Locate every malaria parasite.
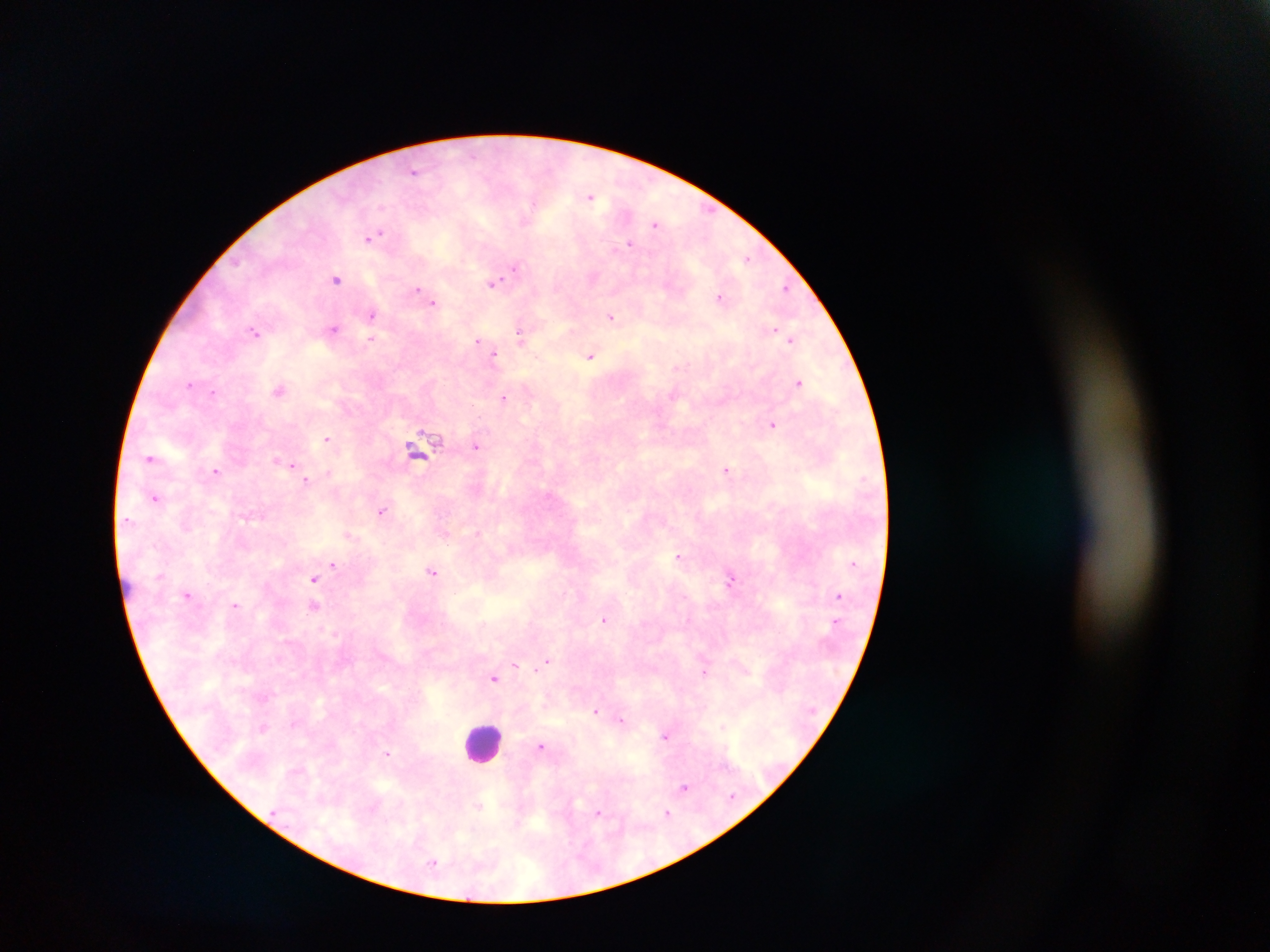
Approximate centers as x y in pixels.
Malaria parasites: 412 169; 591 194; 382 209; 382 232; 371 240; 628 241; 369 243; 749 258; 515 266; 337 280; 493 283; 787 288; 416 289; 719 296; 434 303; 373 313; 611 317; 332 328; 522 328; 258 333; 520 336; 791 337; 371 339; 479 340; 496 353; 591 356; 677 367; 798 382; 190 383; 278 390; 213 392; 504 399; 772 424; 327 438; 427 440; 478 447; 152 457; 274 458; 284 461; 291 464; 727 470; 217 471; 329 472; 307 481; 156 497; 382 512; 349 535; 679 557; 333 564; 433 571; 314 578; 730 578; 187 594; 316 606; 606 622; 548 660; 516 666; 704 673; 495 679; 598 710; 622 719; 722 724; 263 726; 666 736; 543 747; 388 754; 684 787; 732 799; 478 806; 668 813; 436 862.

Leukocyte locations: 478 740. One field of view. Image is 1270×952 pixels. Thick blood smear. Mobile-phone photograph taken through the microscope. Sample from Ghana.